Give the position of every Plasmodium parasite.
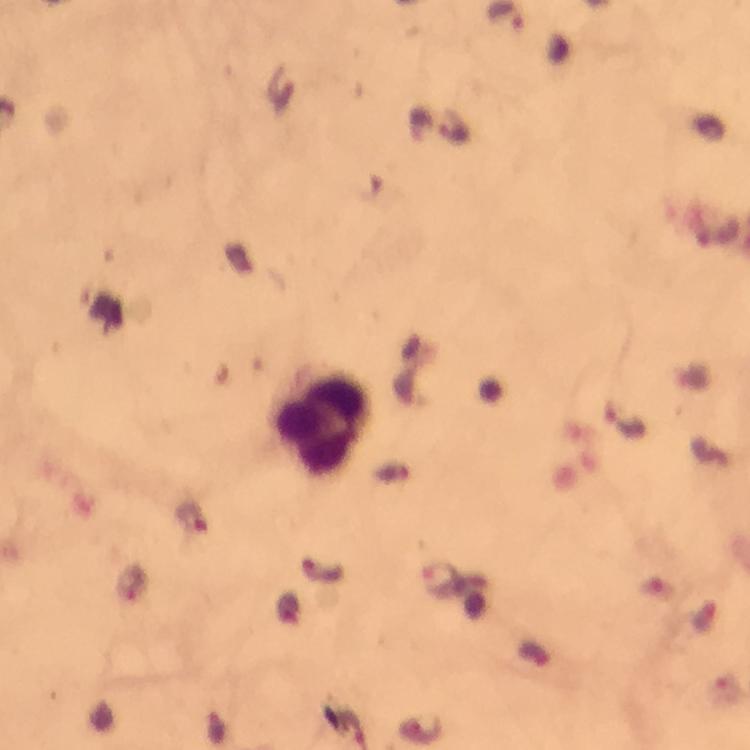

Approximate object centers, in pixels from the top-left corner.
Plasmodium parasites: (x=628, y=423), (x=441, y=580).

Summary:
  - Leukocyte locations: (x=320, y=424)
  - Stain: Giemsa
  - Capture: smartphone photograph through a microscope
  - Preparation: thick blood film
  - Image size: 750×750 pixels
  - Magnification: 100x
  - Context: from a malaria diagnostic workup
  - Immersion oil: used
  - Cropped from: a single field of view